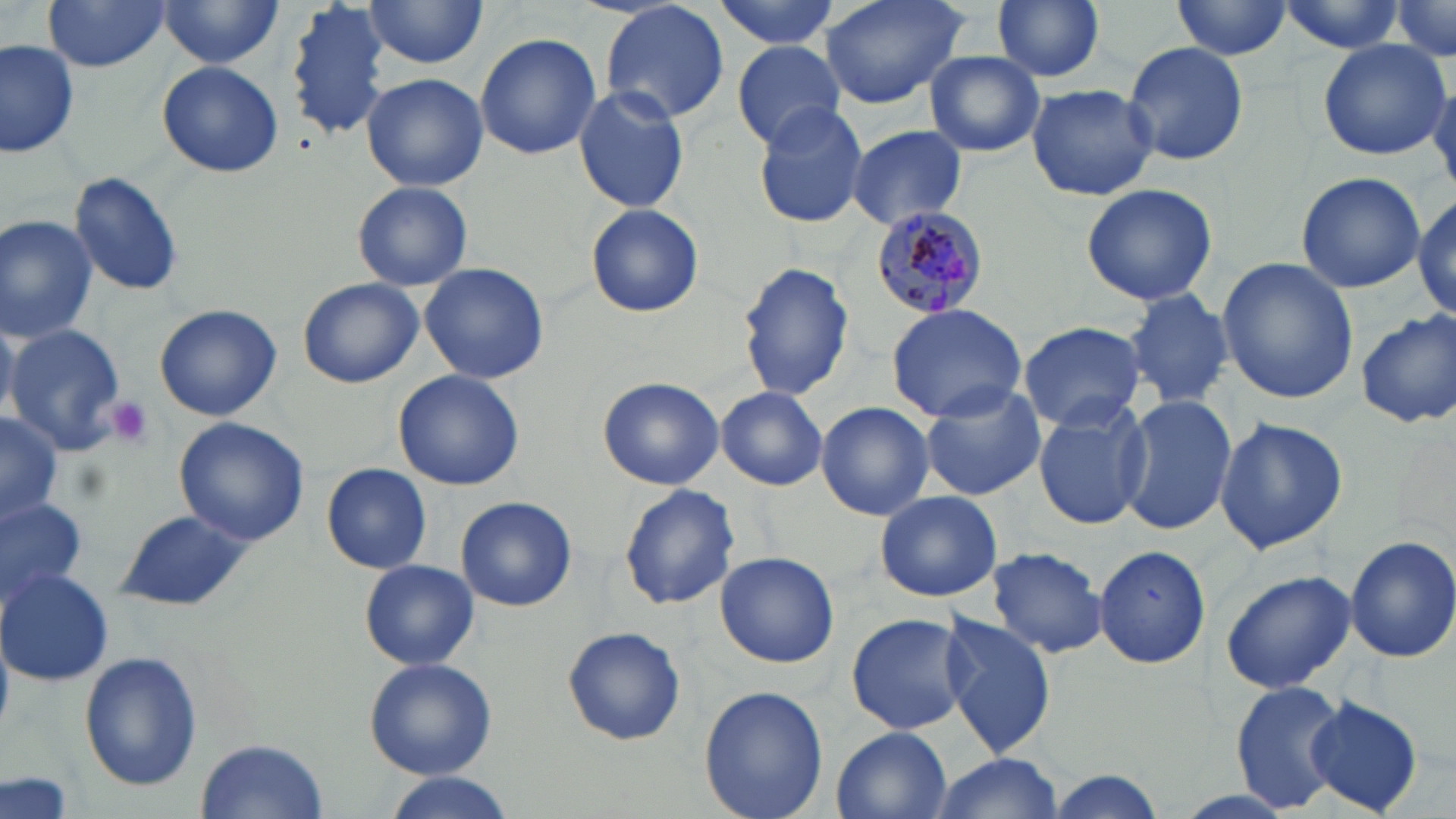

{
  "slide_level_diagnosis": "Plasmodium malariae",
  "magnification": "1000x",
  "plasmodium_malariae_infected_red_blood_cell_locations": "approximate bounding boxes as (x1, y1, x2, y2) in pixels: (871, 207, 992, 318)",
  "field_of_view": "single",
  "platelet_locations": "approximate bounding boxes as (x1, y1, x2, y2) in pixels: (103, 396, 156, 450)",
  "modality": "optical microscopy",
  "image_size": "1456×819 pixels",
  "preparation": "thin blood film",
  "stain": "May-Grünwald-Giemsa",
  "uninfected_red_blood_cell_locations": "approximate bounding boxes as (x1, y1, x2, y2) in pixels: (158, 0, 287, 72), (285, 0, 397, 141), (714, 0, 844, 49), (821, 0, 968, 109), (991, 0, 1105, 83), (1170, 0, 1294, 61), (1272, 0, 1410, 54), (1388, 0, 1456, 63), (43, 1, 170, 71), (363, 1, 488, 69), (598, 1, 731, 125), (476, 32, 601, 159), (2, 37, 80, 160), (1315, 37, 1452, 161), (732, 40, 846, 148), (1124, 41, 1250, 170), (923, 51, 1046, 159), (157, 61, 283, 177), (362, 72, 488, 190), (1026, 82, 1157, 203), (573, 86, 690, 213), (750, 100, 870, 228), (847, 124, 967, 230), (1295, 170, 1425, 293), (70, 173, 184, 298), (351, 181, 474, 292), (1081, 182, 1217, 308), (1414, 192, 1454, 321), (586, 204, 704, 318), (0, 214, 99, 342), (1217, 257, 1358, 404), (735, 261, 856, 401), (418, 262, 550, 386), (297, 277, 424, 388), (1124, 287, 1237, 410), (885, 301, 1028, 426), (154, 303, 282, 421), (1355, 309, 1456, 428), (1017, 320, 1147, 432), (5, 324, 127, 453), (393, 370, 525, 492), (598, 376, 724, 490), (920, 384, 1046, 501), (717, 386, 829, 490), (1119, 393, 1239, 537), (1032, 398, 1155, 532), (816, 401, 935, 521), (0, 408, 61, 528), (1213, 416, 1350, 555), (175, 417, 308, 545), (321, 463, 432, 572), (618, 484, 739, 611), (875, 490, 1001, 602), (0, 496, 86, 599), (454, 497, 578, 612), (115, 510, 250, 613), (1344, 534, 1454, 662), (1092, 543, 1211, 668), (987, 546, 1108, 658), (714, 552, 839, 668), (359, 560, 478, 671), (1, 568, 113, 686), (1221, 571, 1356, 694), (846, 612, 969, 735), (938, 612, 1059, 759), (562, 626, 686, 746), (80, 651, 202, 789), (362, 656, 496, 777), (1231, 683, 1348, 811), (699, 684, 829, 819), (1302, 696, 1426, 817), (831, 727, 954, 818), (196, 739, 329, 817), (932, 753, 1062, 818), (1, 770, 75, 819), (379, 773, 515, 819)"
}